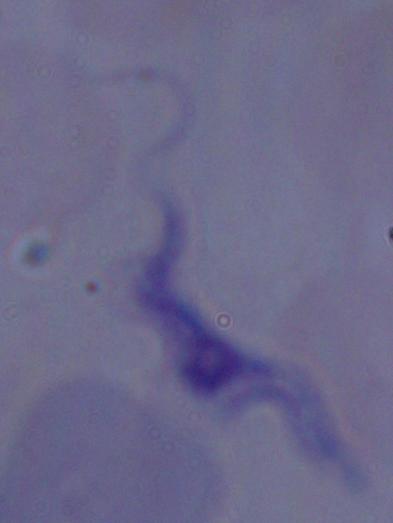
A trypanosome is seen. Captured at 1000x magnification. Photomicrograph.